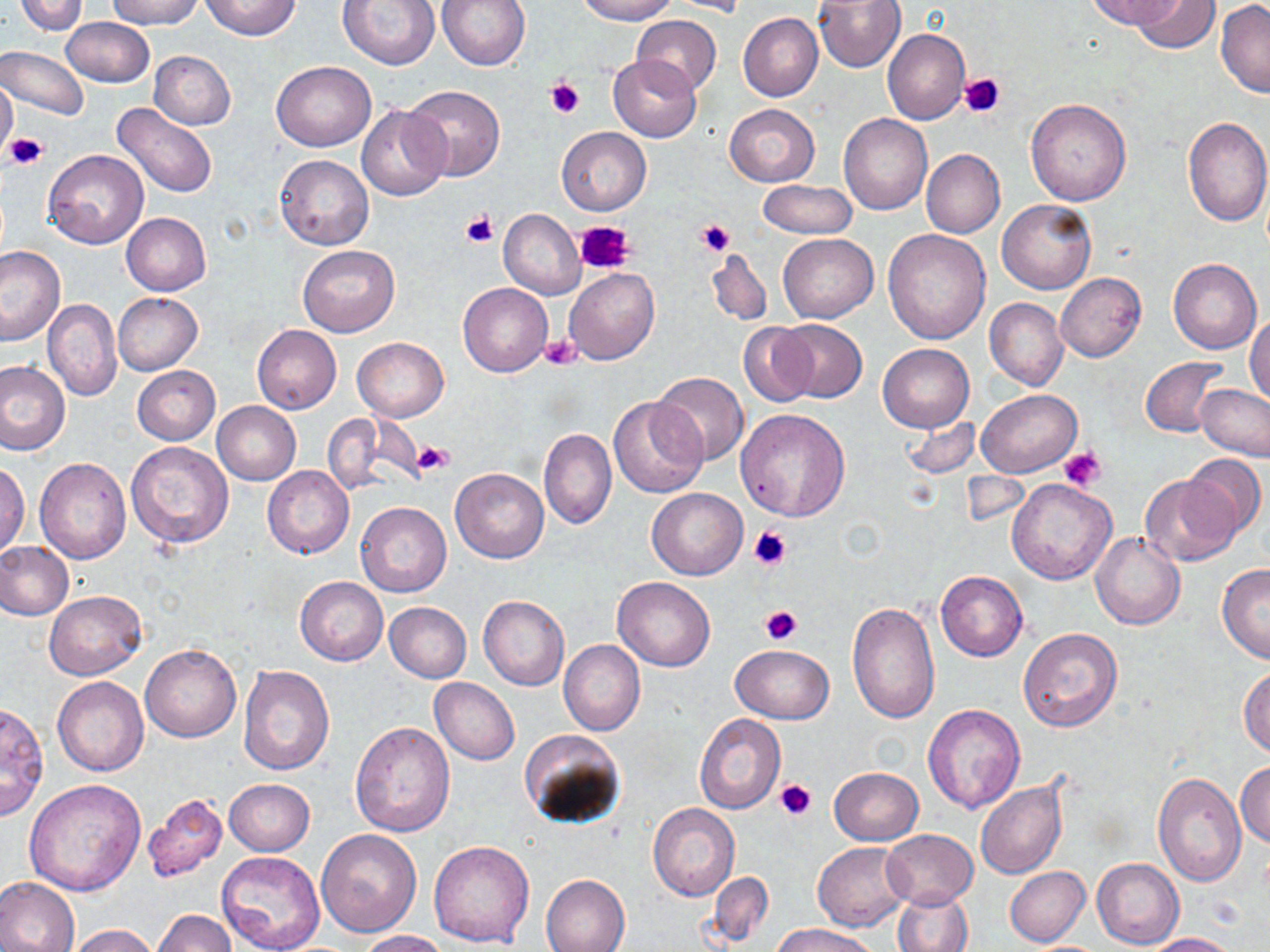
slide-level diagnosis = no evidence of blood parasites
image size = 1270×952 pixels
uninfected red blood cell locations = approximate bounding boxes as named x1/y1/x2/y2 corners in pixels: (x1=14, y1=0, x2=87, y2=35), (x1=107, y1=0, x2=200, y2=28), (x1=202, y1=0, x2=299, y2=39), (x1=337, y1=0, x2=441, y2=70), (x1=437, y1=0, x2=530, y2=69), (x1=574, y1=0, x2=680, y2=24), (x1=668, y1=0, x2=753, y2=17), (x1=814, y1=0, x2=904, y2=72), (x1=1085, y1=0, x2=1180, y2=29), (x1=1131, y1=0, x2=1218, y2=55), (x1=1216, y1=2, x2=1270, y2=98), (x1=739, y1=13, x2=823, y2=101), (x1=631, y1=14, x2=721, y2=95), (x1=61, y1=17, x2=153, y2=87), (x1=883, y1=28, x2=969, y2=123), (x1=1, y1=45, x2=88, y2=121), (x1=149, y1=51, x2=235, y2=129), (x1=607, y1=56, x2=701, y2=142), (x1=271, y1=60, x2=375, y2=151), (x1=0, y1=79, x2=17, y2=157), (x1=404, y1=84, x2=504, y2=180), (x1=1025, y1=98, x2=1131, y2=206), (x1=114, y1=103, x2=218, y2=198), (x1=724, y1=104, x2=819, y2=187), (x1=356, y1=105, x2=451, y2=201), (x1=838, y1=114, x2=932, y2=214), (x1=1183, y1=116, x2=1270, y2=227), (x1=557, y1=126, x2=650, y2=215), (x1=921, y1=149, x2=1005, y2=239), (x1=43, y1=150, x2=148, y2=250), (x1=275, y1=154, x2=373, y2=251), (x1=756, y1=179, x2=857, y2=241), (x1=997, y1=200, x2=1096, y2=294), (x1=498, y1=208, x2=586, y2=299), (x1=121, y1=213, x2=211, y2=296), (x1=883, y1=228, x2=991, y2=344), (x1=778, y1=234, x2=878, y2=323), (x1=297, y1=244, x2=399, y2=336), (x1=0, y1=246, x2=67, y2=346), (x1=705, y1=248, x2=772, y2=325), (x1=1168, y1=259, x2=1261, y2=353), (x1=564, y1=267, x2=659, y2=364), (x1=1056, y1=272, x2=1146, y2=361), (x1=458, y1=282, x2=551, y2=376), (x1=114, y1=293, x2=201, y2=374), (x1=985, y1=298, x2=1068, y2=390), (x1=44, y1=299, x2=121, y2=401), (x1=1247, y1=314, x2=1270, y2=405), (x1=774, y1=319, x2=866, y2=402), (x1=738, y1=321, x2=821, y2=407), (x1=252, y1=325, x2=341, y2=414), (x1=352, y1=336, x2=448, y2=421), (x1=877, y1=342, x2=974, y2=433), (x1=1140, y1=357, x2=1228, y2=437), (x1=0, y1=361, x2=69, y2=455), (x1=133, y1=366, x2=220, y2=445), (x1=652, y1=372, x2=748, y2=466), (x1=1196, y1=384, x2=1270, y2=461), (x1=977, y1=388, x2=1080, y2=477), (x1=608, y1=396, x2=708, y2=500), (x1=213, y1=401, x2=301, y2=483), (x1=735, y1=409, x2=851, y2=522), (x1=323, y1=413, x2=396, y2=497), (x1=902, y1=416, x2=980, y2=479), (x1=539, y1=429, x2=616, y2=530), (x1=126, y1=441, x2=235, y2=549), (x1=1182, y1=452, x2=1266, y2=540), (x1=35, y1=458, x2=130, y2=563), (x1=0, y1=460, x2=30, y2=557), (x1=262, y1=465, x2=353, y2=559), (x1=450, y1=466, x2=549, y2=563), (x1=1141, y1=472, x2=1241, y2=564), (x1=1006, y1=480, x2=1116, y2=585), (x1=647, y1=488, x2=747, y2=579), (x1=356, y1=501, x2=452, y2=597), (x1=1091, y1=533, x2=1185, y2=630), (x1=0, y1=541, x2=74, y2=621), (x1=1216, y1=564, x2=1270, y2=662), (x1=936, y1=570, x2=1027, y2=660), (x1=612, y1=576, x2=715, y2=670), (x1=295, y1=577, x2=388, y2=665), (x1=45, y1=591, x2=146, y2=679), (x1=478, y1=595, x2=570, y2=691), (x1=847, y1=601, x2=940, y2=722), (x1=385, y1=602, x2=471, y2=682), (x1=1018, y1=628, x2=1123, y2=731), (x1=559, y1=640, x2=645, y2=735), (x1=141, y1=645, x2=241, y2=742), (x1=730, y1=645, x2=833, y2=725), (x1=1239, y1=663, x2=1269, y2=758), (x1=239, y1=664, x2=335, y2=775), (x1=53, y1=677, x2=149, y2=776), (x1=429, y1=678, x2=519, y2=765), (x1=0, y1=700, x2=50, y2=822), (x1=923, y1=705, x2=1025, y2=812), (x1=694, y1=715, x2=786, y2=815), (x1=350, y1=722, x2=455, y2=838), (x1=520, y1=729, x2=626, y2=830), (x1=1236, y1=761, x2=1270, y2=848), (x1=830, y1=767, x2=923, y2=845), (x1=1152, y1=773, x2=1247, y2=887), (x1=223, y1=778, x2=315, y2=856), (x1=24, y1=779, x2=145, y2=894), (x1=974, y1=779, x2=1067, y2=880), (x1=140, y1=793, x2=229, y2=886), (x1=648, y1=804, x2=738, y2=900), (x1=316, y1=828, x2=422, y2=937), (x1=881, y1=829, x2=978, y2=909), (x1=429, y1=840, x2=535, y2=948), (x1=812, y1=841, x2=914, y2=930), (x1=216, y1=850, x2=327, y2=952), (x1=1093, y1=856, x2=1184, y2=950), (x1=1005, y1=866, x2=1090, y2=947), (x1=708, y1=871, x2=773, y2=947), (x1=540, y1=874, x2=630, y2=952), (x1=0, y1=878, x2=80, y2=952), (x1=893, y1=889, x2=973, y2=952), (x1=153, y1=909, x2=236, y2=951), (x1=772, y1=923, x2=877, y2=952), (x1=68, y1=924, x2=159, y2=952), (x1=357, y1=930, x2=449, y2=952), (x1=1148, y1=932, x2=1243, y2=952)
platelet locations = approximate bounding boxes as named x1/y1/x2/y2 corners in pixels: (x1=958, y1=73, x2=1005, y2=120), (x1=547, y1=77, x2=584, y2=118), (x1=6, y1=133, x2=47, y2=170), (x1=460, y1=212, x2=498, y2=247), (x1=575, y1=219, x2=634, y2=276), (x1=699, y1=219, x2=735, y2=258), (x1=539, y1=334, x2=581, y2=370), (x1=414, y1=441, x2=453, y2=474), (x1=1059, y1=445, x2=1106, y2=492), (x1=748, y1=525, x2=793, y2=570), (x1=761, y1=605, x2=804, y2=644), (x1=774, y1=777, x2=818, y2=821)
modality = optical microscopy
field of view = single
magnification = 1000x
stain = May-Grünwald-Giemsa
preparation = thin blood film